Locate every Plasmodium falciparum-infected red blood cell.
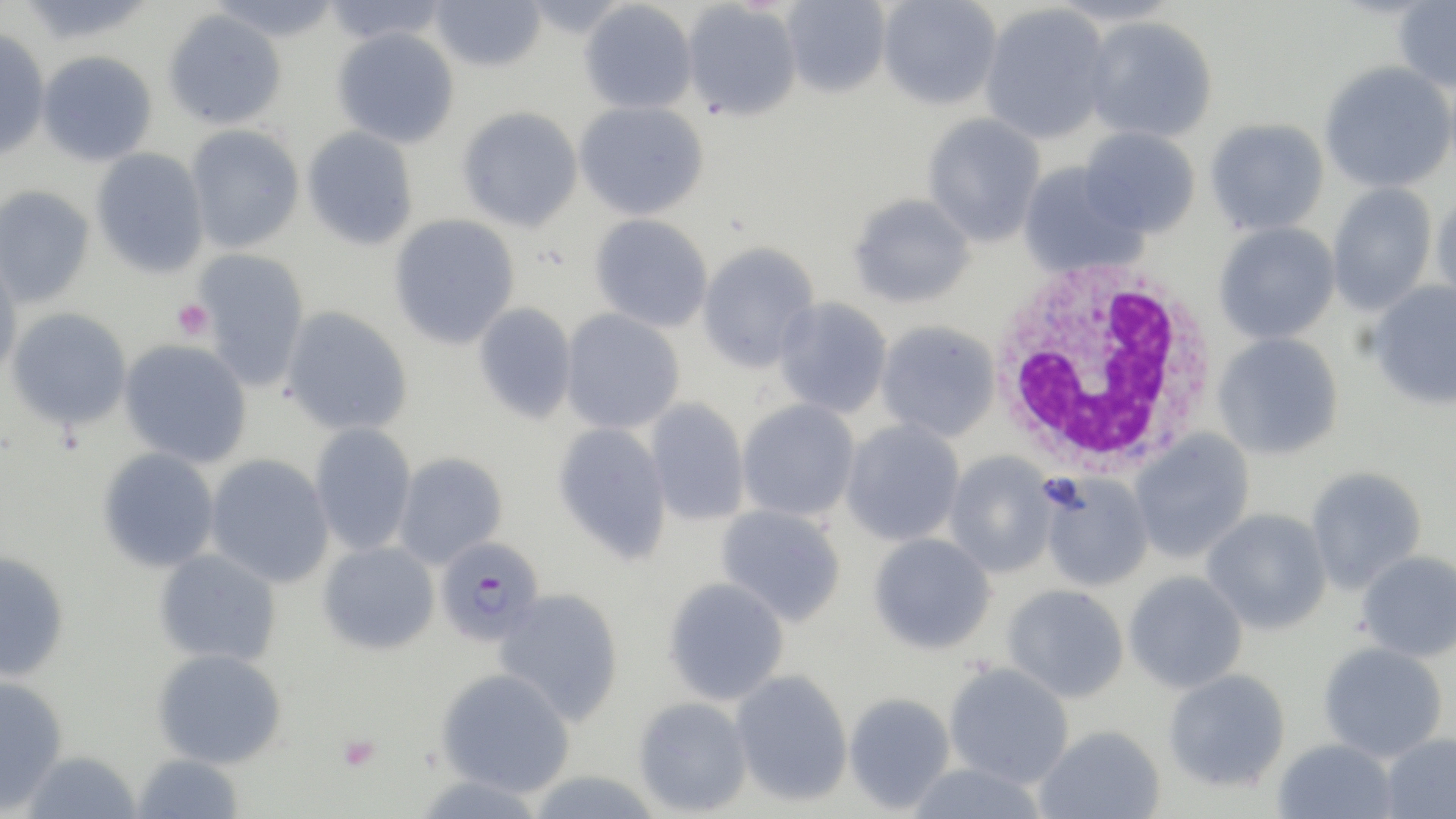
Approximate bounding boxes as [x1, y1, x2, y2] in pixels.
Plasmodium falciparum-infected red blood cells: [434, 536, 544, 647].

White blood cell locations: [986, 260, 1225, 475]. Uninfected red blood cell locations: [320, 0, 451, 46], [428, 0, 547, 72], [780, 0, 891, 98], [877, 0, 1002, 109], [579, 1, 697, 114], [681, 1, 802, 121], [1394, 1, 1456, 93], [979, 3, 1113, 144], [163, 9, 287, 130], [1084, 17, 1218, 143], [0, 27, 51, 161], [332, 27, 460, 148], [37, 51, 158, 166], [1319, 61, 1455, 193], [573, 100, 710, 220], [457, 106, 584, 232], [921, 113, 1046, 247], [1204, 118, 1329, 236], [185, 124, 304, 253], [302, 126, 419, 250], [1078, 126, 1201, 238], [91, 148, 210, 278], [1018, 162, 1146, 277], [1327, 182, 1438, 316], [0, 185, 94, 308], [1431, 190, 1456, 308], [847, 192, 976, 309], [589, 213, 714, 333], [389, 214, 521, 349], [1213, 221, 1340, 345], [696, 241, 820, 372], [193, 248, 311, 391], [0, 254, 23, 384], [1368, 280, 1456, 410], [773, 297, 893, 419], [473, 301, 577, 424], [5, 306, 132, 430], [280, 306, 413, 436], [560, 309, 685, 434], [875, 320, 1001, 442], [1212, 332, 1344, 460], [119, 340, 253, 468], [645, 398, 750, 526], [736, 399, 861, 522], [839, 419, 965, 546], [310, 422, 417, 556], [553, 422, 671, 563], [1129, 430, 1255, 563], [97, 447, 220, 573], [944, 451, 1057, 577], [393, 452, 508, 569], [205, 453, 334, 588], [1305, 465, 1428, 594], [1040, 474, 1153, 593], [715, 504, 847, 627], [1202, 508, 1332, 634], [868, 532, 996, 654], [318, 540, 440, 654], [153, 548, 282, 667], [0, 549, 69, 682], [1355, 550, 1456, 662], [1123, 570, 1248, 693], [663, 576, 790, 706], [1002, 584, 1129, 703], [494, 588, 624, 725], [1318, 642, 1448, 762], [152, 648, 287, 768], [943, 662, 1074, 788], [435, 667, 576, 797], [1163, 668, 1291, 792], [730, 669, 853, 806], [0, 676, 68, 813], [843, 692, 956, 813], [633, 696, 753, 816], [1034, 724, 1165, 818], [1381, 732, 1456, 819], [1273, 738, 1397, 819], [21, 749, 143, 819], [130, 752, 244, 819], [904, 761, 1050, 819]. Platelet locations: [172, 298, 214, 341], [337, 733, 381, 771]. Slide-level diagnosis: Plasmodium falciparum. Image is 1456×819 pixels. Thin blood smear. May-Grünwald-Giemsa stain. Optical microscopy. One field of a larger specimen. 1000x magnification.